Describe the morphology of the red blood cells.
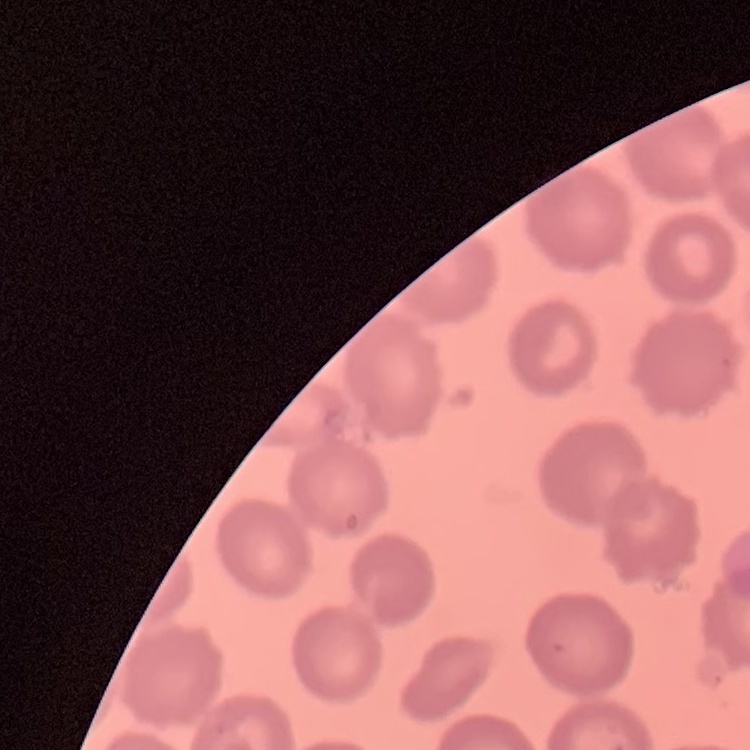

No rouleaux formation.

Summary:
  - Stain: Field's or Giemsa
  - Image type: square crop of a larger photomicrograph
  - Preparation: thin blood smear